Assess the morphology of the erythrocytes.
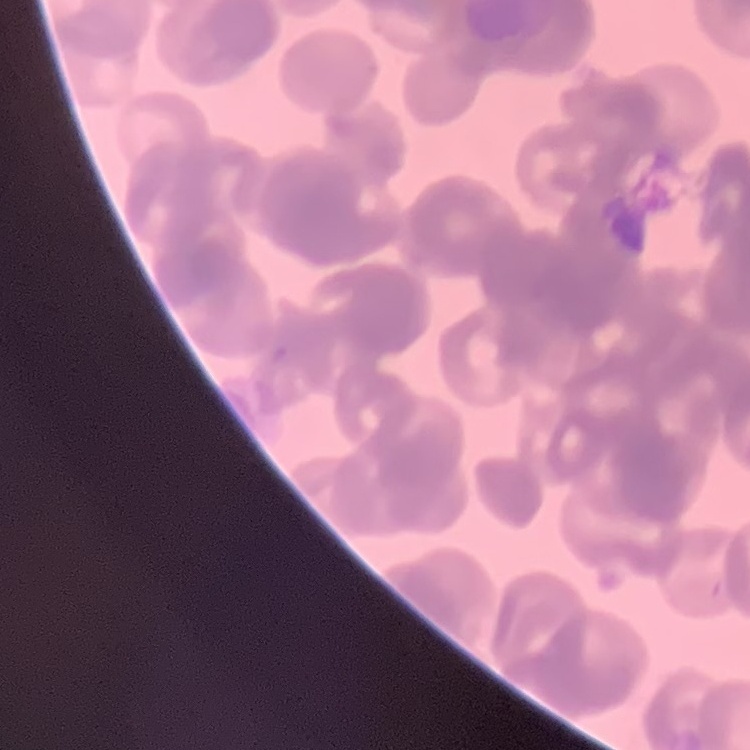

Rouleaux formation.

Thin blood film. Field's or Giemsa stain. Square crop of a larger photomicrograph.